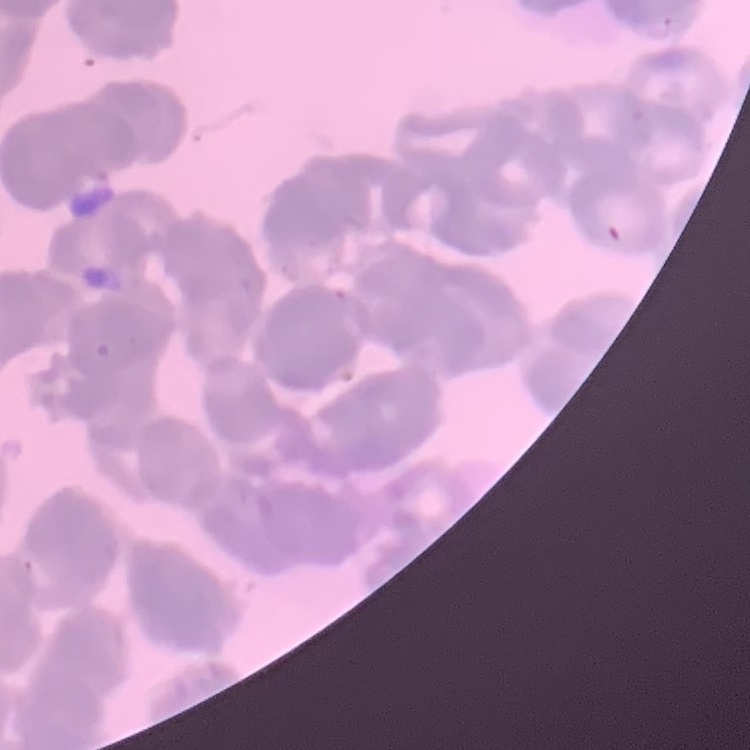
Summary:
  - Erythrocyte morphology: rouleaux formation
  - Preparation: thin blood film
  - Image type: square crop of a larger photomicrograph
  - Stain: Field's or Giemsa